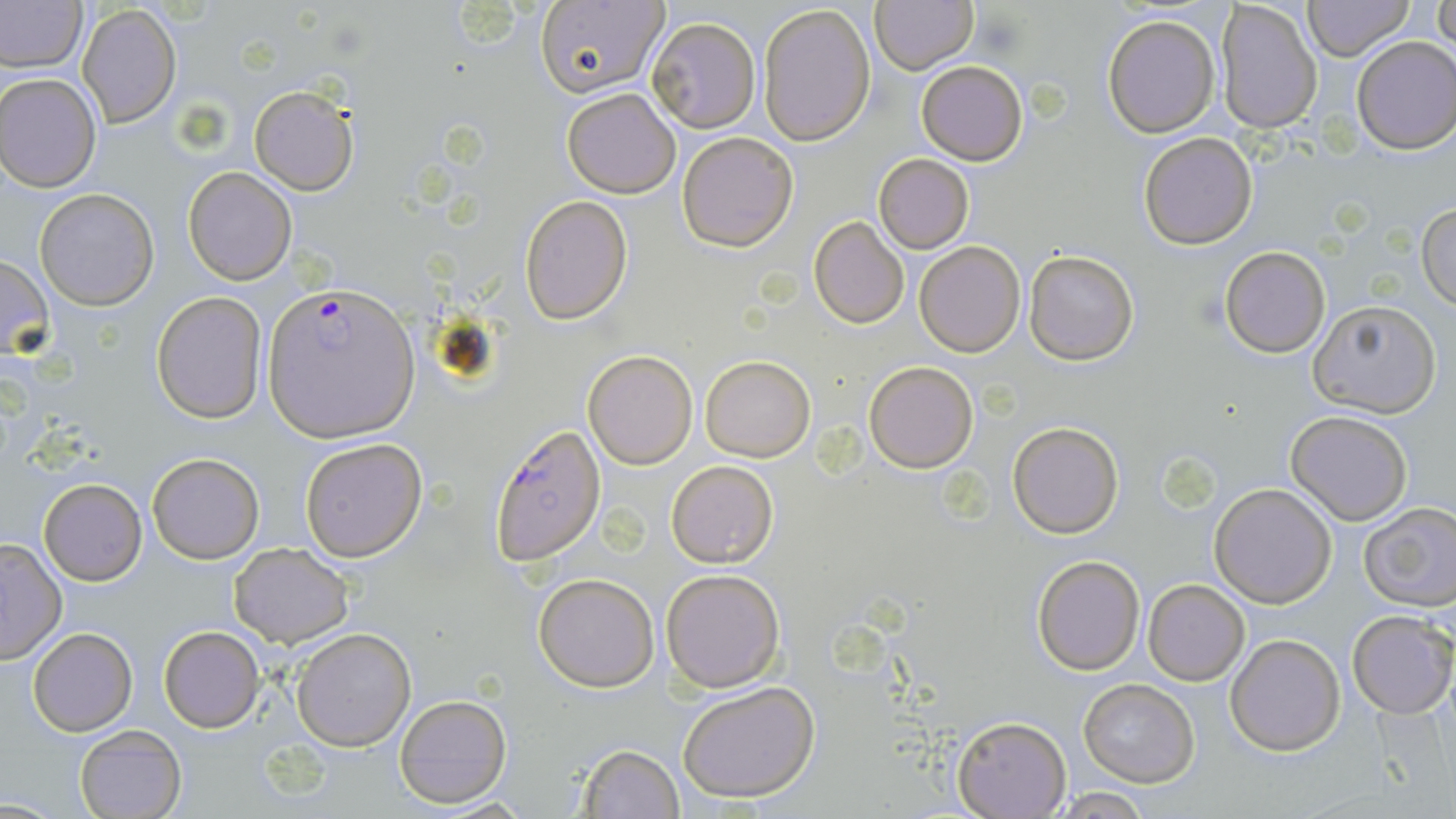 Approximate bounding boxes as named x1/y1/x2/y2 corners in pixels. Uninfected red blood cell locations: (x1=869, y1=0, x2=977, y2=74), (x1=1301, y1=0, x2=1415, y2=61), (x1=0, y1=1, x2=86, y2=74), (x1=538, y1=1, x2=671, y2=98), (x1=1216, y1=2, x2=1323, y2=134), (x1=756, y1=3, x2=876, y2=148), (x1=1430, y1=3, x2=1456, y2=51), (x1=77, y1=4, x2=182, y2=129), (x1=1101, y1=15, x2=1220, y2=138), (x1=647, y1=16, x2=760, y2=132), (x1=1351, y1=36, x2=1456, y2=155), (x1=916, y1=60, x2=1028, y2=165), (x1=0, y1=72, x2=101, y2=191), (x1=249, y1=85, x2=358, y2=194), (x1=563, y1=88, x2=681, y2=198), (x1=676, y1=130, x2=799, y2=251), (x1=1137, y1=131, x2=1259, y2=249), (x1=874, y1=153, x2=974, y2=254), (x1=184, y1=167, x2=298, y2=285), (x1=35, y1=188, x2=160, y2=311), (x1=519, y1=195, x2=633, y2=324), (x1=1418, y1=199, x2=1456, y2=311), (x1=808, y1=216, x2=910, y2=329), (x1=915, y1=240, x2=1025, y2=357), (x1=1217, y1=247, x2=1332, y2=358), (x1=1023, y1=249, x2=1140, y2=366), (x1=0, y1=253, x2=55, y2=360), (x1=152, y1=292, x2=268, y2=425), (x1=1306, y1=300, x2=1441, y2=419), (x1=583, y1=350, x2=698, y2=469), (x1=701, y1=354, x2=816, y2=461), (x1=864, y1=361, x2=978, y2=472), (x1=1286, y1=411, x2=1412, y2=525), (x1=1007, y1=420, x2=1124, y2=538), (x1=299, y1=438, x2=428, y2=561), (x1=147, y1=453, x2=264, y2=564), (x1=666, y1=460, x2=777, y2=568), (x1=39, y1=479, x2=147, y2=586), (x1=1209, y1=483, x2=1337, y2=607), (x1=1357, y1=502, x2=1456, y2=611), (x1=0, y1=540, x2=67, y2=665), (x1=229, y1=542, x2=354, y2=648), (x1=1030, y1=555, x2=1145, y2=675), (x1=661, y1=568, x2=785, y2=693), (x1=532, y1=572, x2=660, y2=693), (x1=1142, y1=578, x2=1250, y2=686), (x1=1347, y1=611, x2=1455, y2=717), (x1=158, y1=625, x2=266, y2=733), (x1=27, y1=627, x2=138, y2=736), (x1=291, y1=627, x2=417, y2=751), (x1=1225, y1=634, x2=1344, y2=755), (x1=1076, y1=678, x2=1200, y2=786), (x1=675, y1=680, x2=822, y2=804), (x1=393, y1=693, x2=511, y2=809), (x1=951, y1=716, x2=1071, y2=818), (x1=74, y1=725, x2=187, y2=818), (x1=576, y1=742, x2=684, y2=818), (x1=1050, y1=790, x2=1156, y2=818). Plasmodium falciparum-infected red blood cell locations: (x1=264, y1=280, x2=420, y2=442), (x1=489, y1=424, x2=607, y2=567). Slide-level diagnosis: Plasmodium falciparum. Light microscopy. One field of a larger specimen. 1000x magnification. Thin blood film. May-Grünwald-Giemsa stain. Image is 1456×819 pixels.